Outline platelets.
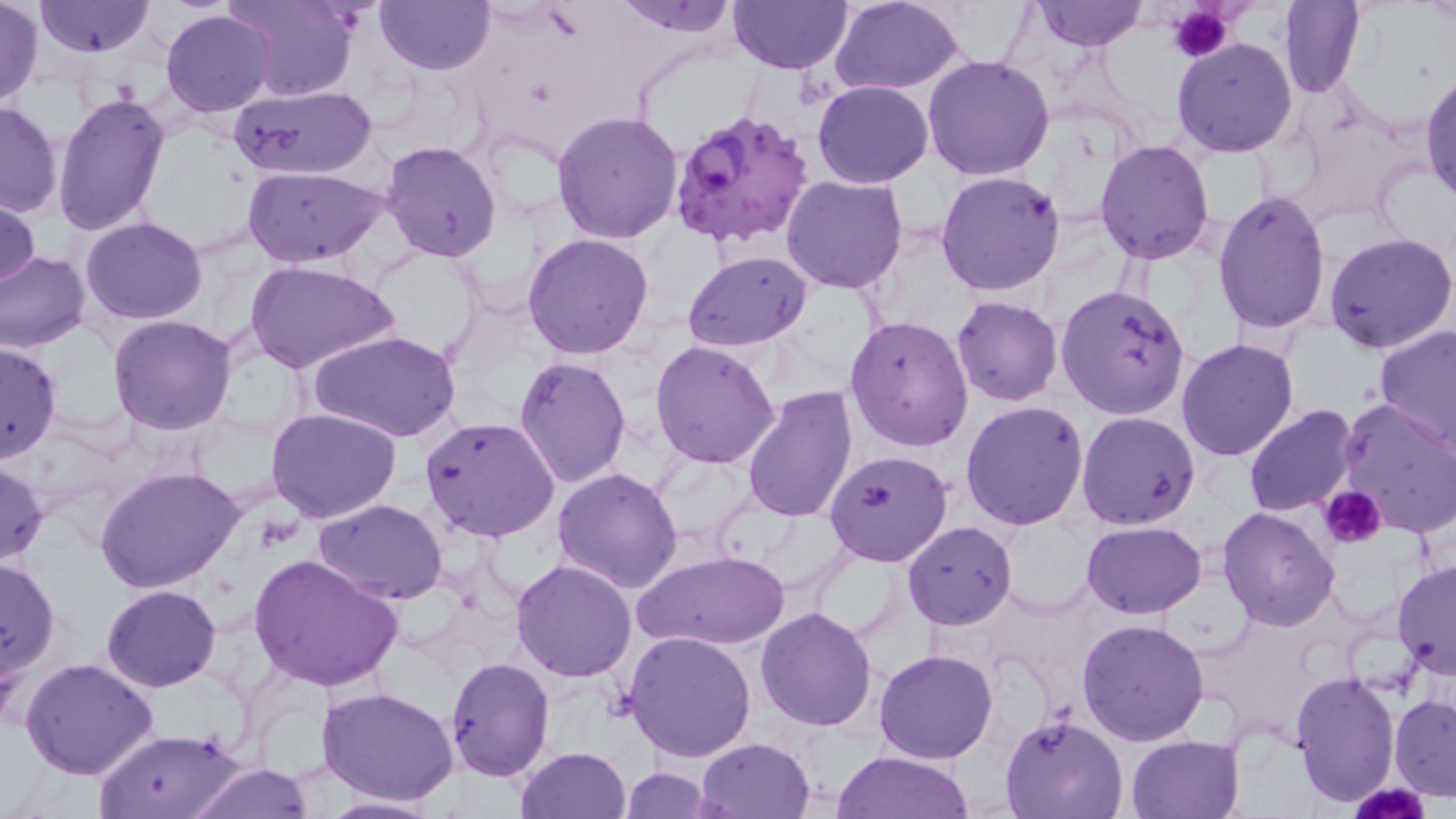
Approximate bounding boxes as named x1/y1/x2/y2 corners in pixels.
Platelets: (x1=1168, y1=3, x2=1234, y2=63), (x1=1320, y1=485, x2=1387, y2=547), (x1=1352, y1=781, x2=1427, y2=819).

Summary:
  - Uninfected red blood cell locations: (x1=227, y1=0, x2=360, y2=100), (x1=374, y1=0, x2=494, y2=73), (x1=611, y1=0, x2=743, y2=36), (x1=828, y1=0, x2=968, y2=94), (x1=1030, y1=0, x2=1147, y2=50), (x1=1278, y1=0, x2=1366, y2=99), (x1=34, y1=1, x2=155, y2=56), (x1=728, y1=1, x2=853, y2=74), (x1=2, y1=2, x2=42, y2=103), (x1=161, y1=9, x2=277, y2=116), (x1=1171, y1=37, x2=1298, y2=157), (x1=923, y1=54, x2=1056, y2=181), (x1=1420, y1=68, x2=1455, y2=204), (x1=812, y1=80, x2=934, y2=187), (x1=228, y1=84, x2=379, y2=180), (x1=53, y1=90, x2=170, y2=236), (x1=0, y1=100, x2=63, y2=219), (x1=551, y1=110, x2=684, y2=245), (x1=380, y1=139, x2=503, y2=261), (x1=1094, y1=139, x2=1215, y2=263), (x1=240, y1=166, x2=389, y2=267), (x1=936, y1=169, x2=1067, y2=297), (x1=782, y1=175, x2=909, y2=294), (x1=1, y1=189, x2=42, y2=293), (x1=1213, y1=190, x2=1332, y2=335), (x1=80, y1=217, x2=208, y2=324), (x1=523, y1=232, x2=654, y2=358), (x1=1324, y1=232, x2=1456, y2=354), (x1=682, y1=250, x2=812, y2=350), (x1=0, y1=251, x2=89, y2=353), (x1=245, y1=261, x2=399, y2=374), (x1=1055, y1=284, x2=1191, y2=418), (x1=951, y1=295, x2=1063, y2=406), (x1=844, y1=313, x2=973, y2=452), (x1=108, y1=315, x2=236, y2=435), (x1=1375, y1=324, x2=1456, y2=450), (x1=308, y1=330, x2=460, y2=443), (x1=1176, y1=337, x2=1300, y2=462), (x1=0, y1=339, x2=62, y2=462), (x1=651, y1=340, x2=780, y2=469), (x1=514, y1=356, x2=632, y2=488), (x1=740, y1=383, x2=857, y2=524), (x1=1333, y1=399, x2=1456, y2=538), (x1=961, y1=401, x2=1089, y2=532), (x1=1243, y1=404, x2=1360, y2=516), (x1=266, y1=408, x2=402, y2=523), (x1=1076, y1=411, x2=1200, y2=529), (x1=419, y1=417, x2=561, y2=541), (x1=824, y1=449, x2=952, y2=566), (x1=0, y1=460, x2=48, y2=568), (x1=96, y1=466, x2=245, y2=594), (x1=552, y1=467, x2=684, y2=593), (x1=313, y1=499, x2=450, y2=605), (x1=1218, y1=505, x2=1341, y2=630), (x1=1081, y1=520, x2=1206, y2=618), (x1=901, y1=521, x2=1017, y2=629), (x1=808, y1=548, x2=908, y2=642), (x1=632, y1=549, x2=788, y2=650), (x1=249, y1=552, x2=406, y2=693), (x1=1, y1=557, x2=60, y2=681), (x1=511, y1=558, x2=637, y2=682), (x1=1392, y1=558, x2=1456, y2=681), (x1=101, y1=584, x2=219, y2=691), (x1=755, y1=606, x2=879, y2=731), (x1=1077, y1=617, x2=1210, y2=744), (x1=623, y1=630, x2=757, y2=761), (x1=876, y1=649, x2=998, y2=763), (x1=443, y1=656, x2=554, y2=782), (x1=20, y1=657, x2=160, y2=780), (x1=1291, y1=671, x2=1401, y2=806), (x1=317, y1=686, x2=460, y2=806), (x1=1390, y1=694, x2=1456, y2=799), (x1=1001, y1=712, x2=1128, y2=819), (x1=93, y1=727, x2=246, y2=818), (x1=1125, y1=734, x2=1242, y2=818), (x1=695, y1=737, x2=816, y2=819), (x1=517, y1=747, x2=633, y2=818), (x1=831, y1=751, x2=979, y2=819), (x1=186, y1=763, x2=316, y2=818), (x1=619, y1=766, x2=715, y2=818), (x1=311, y1=794, x2=445, y2=818)
  - Plasmodium falciparum-infected red blood cell locations: (x1=667, y1=106, x2=817, y2=249)
  - Slide-level diagnosis: Plasmodium falciparum
  - Preparation: thin blood smear
  - Field of view: single
  - Image size: 1456×819 pixels
  - Stain: May-Grünwald-Giemsa
  - Magnification: 1000x
  - Modality: optical microscopy